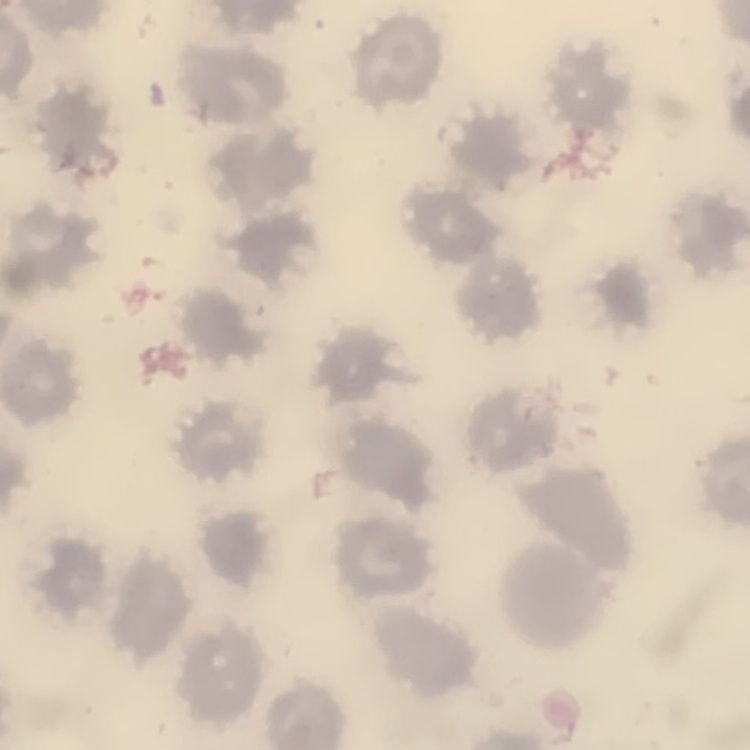

{
  "erythrocyte_morphology": "no rouleaux formation",
  "stain": "Field's or Giemsa",
  "image_type": "one tile cut from a larger photomicrograph",
  "preparation": "thin blood film"
}